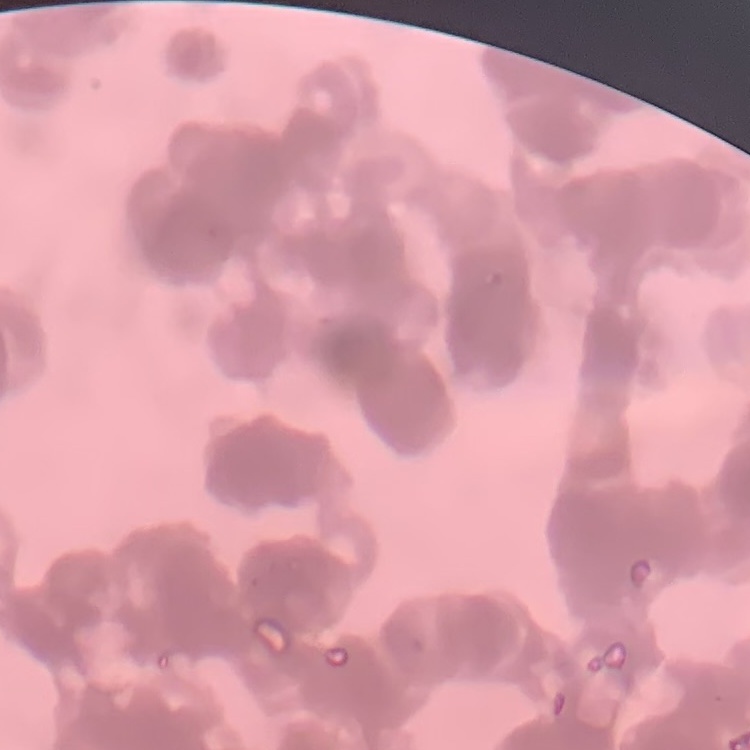

erythrocyte morphology = rouleaux formation
image type = one tile cut from a larger photomicrograph
stain = Field's or Giemsa
preparation = thin blood film